Locate and identify every blood parasite.
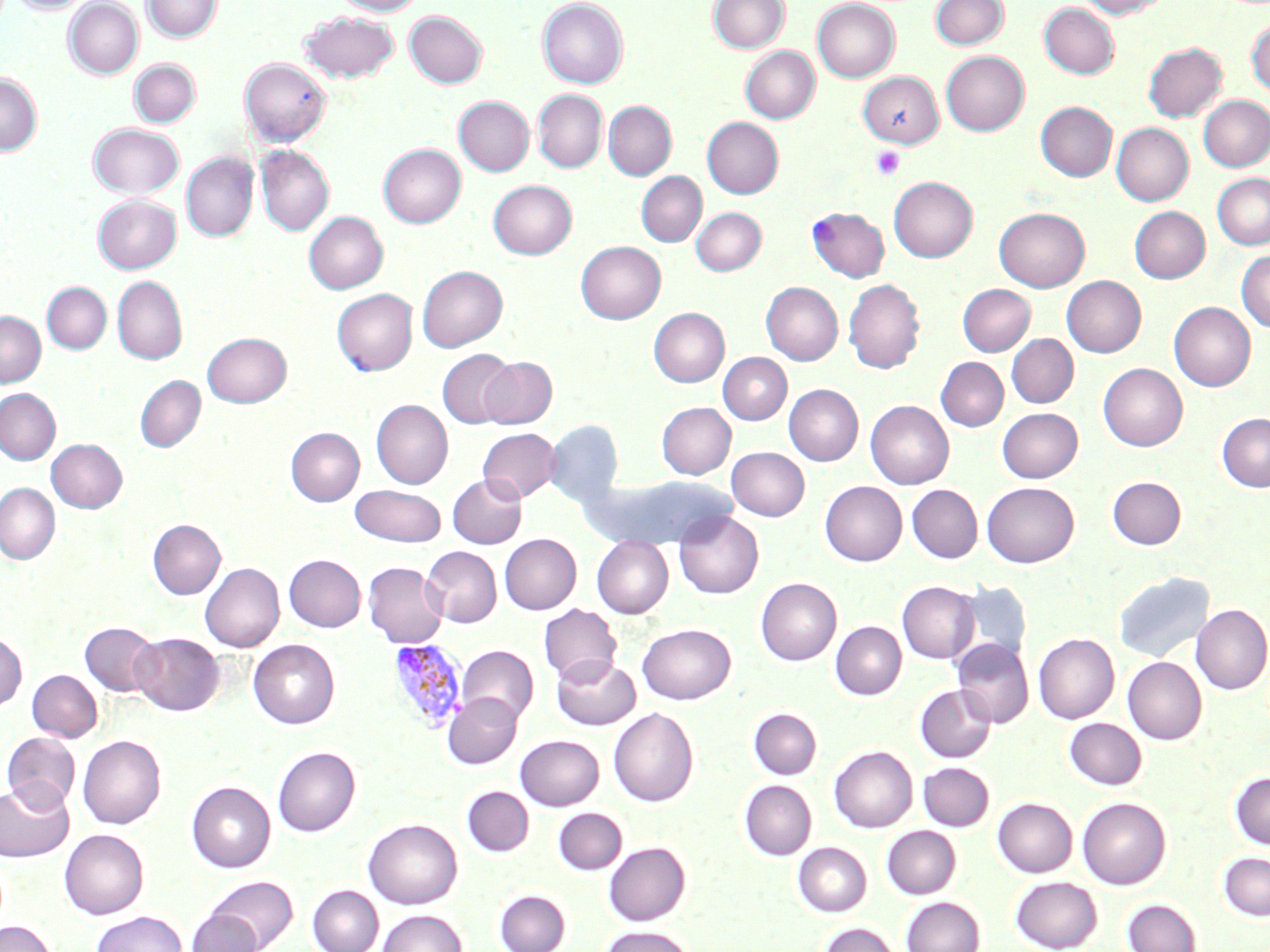

Approximate bounding boxes as (x1, y1, x2, y2) in pixels.
Plasmodium vivax-infected red blood cells: (387, 639, 467, 733).
No Plasmodium falciparum, Plasmodium ovale, Plasmodium malariae, Babesia divergens, or Trypanosoma brucei observed.

slide-level diagnosis = Plasmodium vivax
field of view = one of a larger specimen
platelet locations = approximate bounding boxes as (x1, y1, x2, y2) in pixels: (872, 146, 905, 180)
image size = 1270×952 pixels
modality = light microscopy
preparation = thin blood film
stain = May-Grünwald-Giemsa
uninfected red blood cell locations = approximate bounding boxes as (x1, y1, x2, y2) in pixels: (9, 0, 93, 14), (142, 0, 221, 42), (333, 0, 425, 16), (537, 0, 628, 89), (708, 0, 789, 53), (812, 0, 900, 82), (930, 0, 1009, 50), (1078, 0, 1168, 18), (63, 1, 143, 79), (1039, 2, 1119, 78), (300, 11, 400, 83), (405, 11, 487, 88), (1246, 18, 1270, 98), (1144, 42, 1227, 122), (740, 46, 820, 123), (941, 51, 1030, 136), (240, 57, 332, 145), (129, 59, 200, 127), (857, 71, 943, 148), (0, 72, 42, 156), (533, 90, 607, 173), (1199, 95, 1270, 171), (453, 96, 534, 176), (603, 101, 676, 179), (1036, 101, 1117, 181), (702, 117, 783, 198), (89, 123, 184, 198), (1111, 123, 1194, 206), (378, 143, 466, 228), (255, 145, 334, 236), (181, 152, 258, 242), (636, 172, 706, 246), (1212, 173, 1270, 249), (888, 176, 978, 262), (488, 180, 577, 259), (93, 194, 181, 274), (1130, 206, 1210, 283), (691, 207, 766, 275), (807, 207, 890, 282), (994, 207, 1090, 292), (304, 211, 388, 294), (576, 241, 666, 324), (1236, 250, 1270, 332), (417, 265, 507, 351), (1062, 275, 1146, 357), (112, 276, 186, 365), (843, 278, 925, 374), (42, 282, 111, 354), (761, 282, 843, 365), (957, 284, 1035, 356), (332, 289, 418, 375), (1169, 301, 1256, 391), (649, 307, 729, 386), (0, 311, 45, 387), (202, 332, 291, 407), (1007, 334, 1078, 407), (437, 349, 518, 428), (718, 353, 792, 425), (479, 357, 556, 428), (935, 357, 1008, 431), (1099, 363, 1187, 450), (135, 375, 205, 452), (784, 384, 863, 466), (0, 389, 60, 464), (371, 400, 453, 489), (866, 400, 954, 488), (656, 402, 735, 479), (997, 407, 1083, 482), (1217, 413, 1270, 491), (545, 419, 623, 508), (286, 427, 364, 506), (478, 428, 560, 502), (47, 439, 127, 513), (726, 447, 809, 520), (447, 474, 526, 548), (591, 475, 733, 547), (1108, 477, 1186, 548), (820, 481, 907, 565), (982, 481, 1079, 567), (0, 483, 60, 564), (350, 485, 446, 547), (907, 485, 982, 563), (674, 511, 763, 598), (148, 519, 225, 599), (500, 534, 581, 614), (592, 537, 673, 618), (421, 546, 502, 627), (284, 554, 366, 632), (363, 561, 448, 648), (200, 562, 284, 652), (1114, 571, 1214, 663), (756, 578, 841, 665), (956, 580, 1032, 666), (897, 581, 979, 663), (539, 604, 621, 685), (1191, 604, 1270, 694), (830, 621, 906, 699), (80, 622, 160, 696), (637, 623, 735, 704), (0, 633, 26, 711), (130, 633, 224, 715), (1033, 633, 1119, 723), (952, 638, 1034, 728), (249, 639, 339, 729), (457, 645, 538, 725), (551, 655, 640, 730), (1123, 657, 1206, 744), (27, 670, 102, 742), (915, 685, 996, 762), (443, 693, 522, 769), (609, 708, 698, 807), (749, 708, 821, 779), (1065, 718, 1146, 789), (2, 732, 79, 810), (77, 734, 166, 829), (515, 735, 604, 810), (273, 746, 360, 836), (829, 746, 917, 833), (918, 762, 994, 830), (1230, 771, 1270, 850), (0, 780, 73, 862), (740, 780, 816, 860), (186, 781, 275, 872), (462, 786, 533, 856), (1077, 797, 1170, 889), (993, 798, 1077, 877), (554, 808, 626, 875), (363, 818, 462, 909), (882, 826, 961, 898), (59, 829, 149, 919), (604, 842, 690, 925), (793, 842, 871, 916), (1219, 852, 1270, 921), (205, 876, 297, 951), (1011, 876, 1102, 951), (307, 885, 383, 952), (494, 889, 570, 952), (901, 897, 984, 952), (1123, 899, 1202, 952), (378, 909, 467, 952), (91, 910, 187, 952), (188, 910, 263, 952), (0, 920, 56, 952), (819, 922, 900, 952), (600, 925, 695, 952)
magnification = 1000x